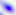

400x magnification. Toxoplasma gondii is shown. Photomicrograph.